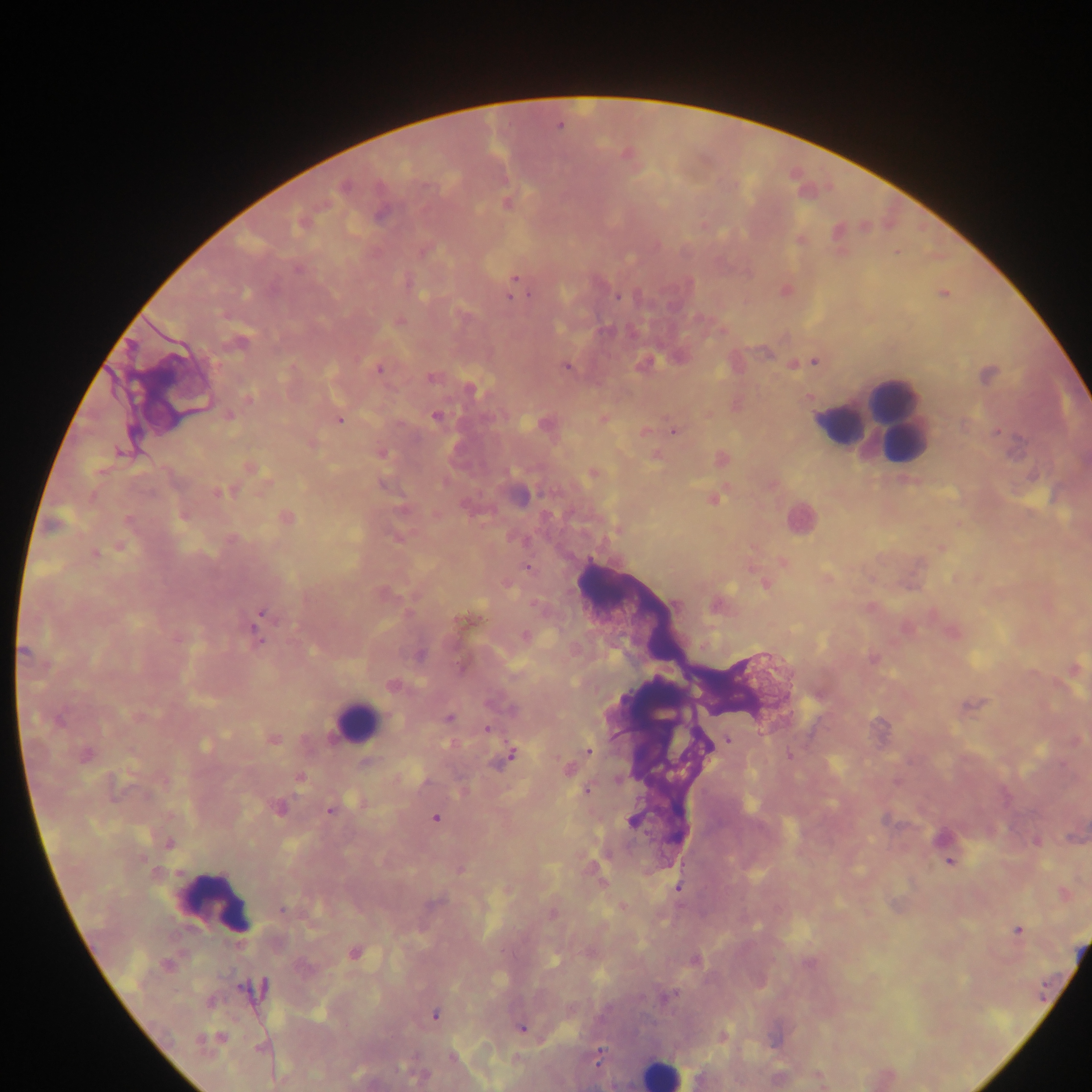

{
  "capture": "mobile-phone photograph through a microscope",
  "country": "Ghana",
  "plasmodium_parasite_locations": "approximate centers as x y in pixels: 514 277; 619 296; 509 297; 814 361; 566 364; 377 368; 431 378; 248 399; 228 416; 434 417; 338 418; 644 430; 673 430; 996 432; 120 452; 251 468; 217 493; 711 498; 616 530; 95 554; 255 624; 260 641; 872 658; 486 729; 272 739; 727 741; 590 752; 512 754; 788 754; 569 770; 301 777; 619 780; 588 789; 280 809; 330 810; 434 818; 950 861; 678 887; 282 910; 1018 931; 353 954; 434 1015; 523 1029; 258 1047; 599 1057; 819 1076; 821 1083",
  "field_of_view": "single",
  "image_size": "1092×1092 pixels",
  "preparation": "thick blood smear",
  "leukocyte_locations": "approximate centers as x y in pixels: 896 393; 837 426; 905 445; 357 718; 217 905; 664 1073"
}